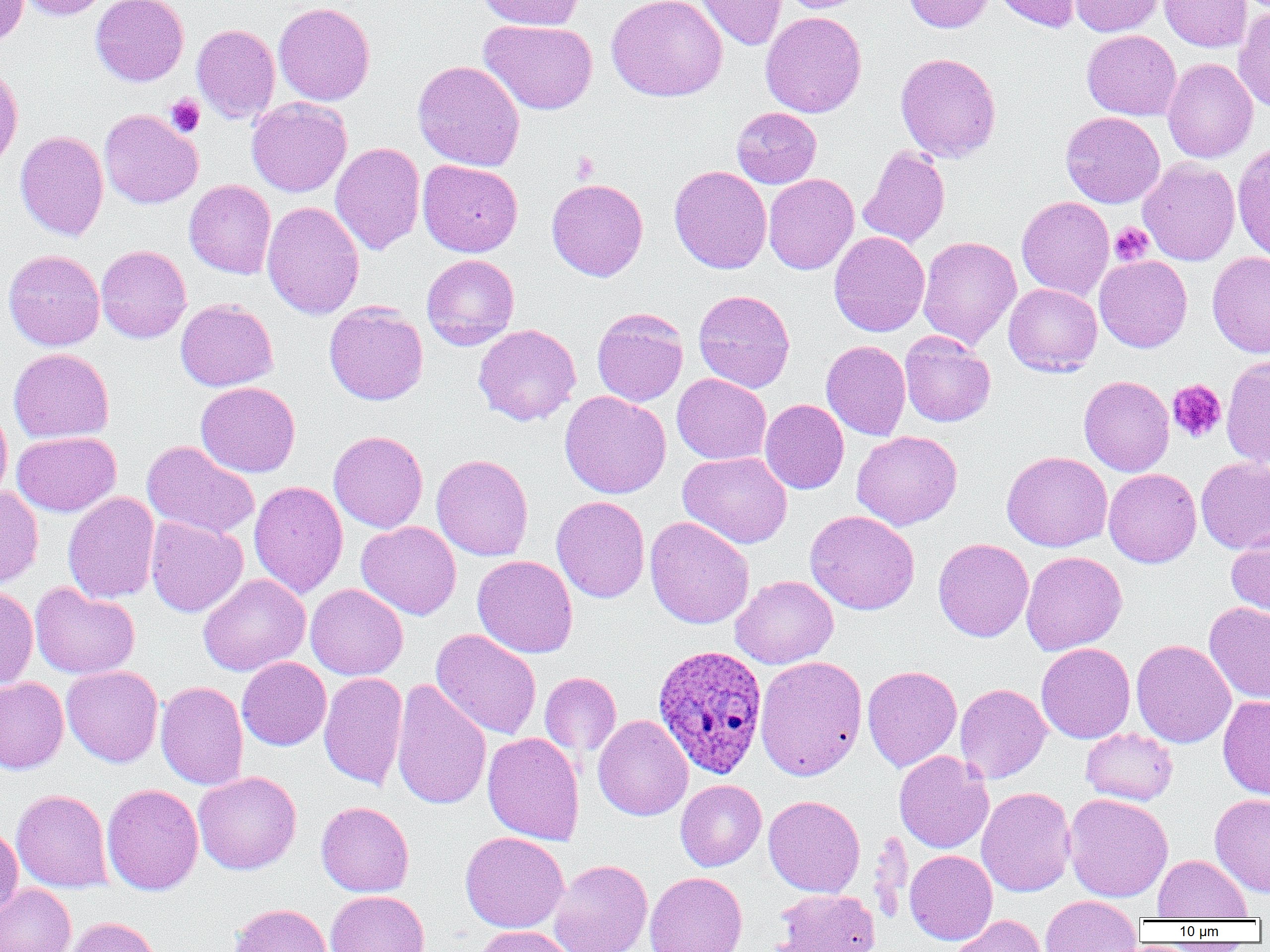

{
  "slide_level_diagnosis": "Plasmodium ovale",
  "image_size": "1270×952 pixels",
  "plasmodium_ovale_infected_red_blood_cell_locations": "approximate bounding boxes as [x1, y1, x2, y2] in pixels: [652, 644, 768, 778]",
  "uninfected_red_blood_cell_locations": "approximate bounding boxes as [x1, y1, x2, y2] in pixels: [0, 0, 29, 48], [18, 0, 112, 21], [91, 0, 189, 86], [477, 0, 585, 30], [606, 0, 728, 102], [696, 0, 787, 50], [778, 0, 872, 13], [902, 0, 995, 34], [993, 0, 1082, 32], [1070, 0, 1166, 36], [1159, 0, 1252, 52], [273, 2, 375, 106], [1234, 7, 1270, 112], [760, 11, 867, 118], [479, 19, 598, 115], [192, 24, 280, 123], [1082, 30, 1181, 120], [895, 52, 1002, 162], [1162, 58, 1258, 163], [413, 60, 525, 171], [0, 63, 23, 173], [247, 97, 352, 198], [731, 107, 822, 188], [99, 109, 203, 208], [1061, 111, 1165, 208], [15, 130, 108, 241], [330, 142, 425, 255], [1233, 145, 1270, 261], [858, 146, 950, 248], [1138, 158, 1240, 266], [417, 159, 523, 257], [669, 165, 772, 274], [763, 173, 859, 275], [546, 178, 648, 281], [184, 180, 276, 279], [1016, 196, 1114, 300], [262, 201, 365, 319], [829, 231, 930, 337], [917, 236, 1021, 350], [96, 245, 191, 343], [3, 250, 105, 351], [1207, 251, 1270, 357], [421, 254, 519, 350], [1094, 255, 1192, 353], [1004, 283, 1102, 376], [693, 289, 795, 392], [175, 298, 278, 391], [324, 302, 428, 405], [592, 308, 689, 407], [473, 324, 581, 426], [900, 331, 996, 427], [821, 341, 911, 440], [8, 348, 114, 443], [1221, 355, 1270, 467], [672, 373, 771, 464], [1079, 375, 1174, 476], [196, 381, 300, 477], [560, 391, 671, 499], [760, 399, 849, 494], [0, 403, 12, 504], [852, 430, 963, 530], [12, 431, 121, 516], [329, 431, 428, 533], [142, 441, 260, 540], [1002, 451, 1112, 552], [678, 452, 792, 548], [431, 454, 533, 561], [1196, 457, 1270, 554], [1104, 468, 1201, 568], [249, 480, 348, 598], [0, 486, 43, 589], [63, 492, 160, 604], [551, 496, 650, 603], [805, 510, 920, 615], [145, 515, 248, 617], [645, 516, 754, 629], [356, 521, 461, 620], [1226, 528, 1270, 619], [933, 538, 1034, 642], [1021, 551, 1127, 655], [472, 555, 578, 658], [198, 574, 311, 676], [730, 575, 839, 669], [29, 582, 140, 679], [305, 584, 408, 680], [0, 587, 38, 689], [1204, 601, 1270, 703], [431, 629, 542, 740], [1131, 639, 1236, 748], [1036, 642, 1135, 743], [754, 655, 867, 780], [237, 657, 331, 750], [62, 665, 164, 767], [862, 665, 962, 772], [539, 672, 621, 757], [319, 673, 409, 790], [0, 678, 69, 774], [391, 678, 491, 810], [155, 681, 248, 790], [955, 683, 1051, 783], [1218, 694, 1270, 799], [593, 715, 693, 821], [1080, 728, 1178, 805], [482, 732, 585, 846], [894, 751, 994, 854], [193, 771, 301, 874], [675, 779, 766, 871], [101, 783, 203, 895], [976, 786, 1076, 897], [11, 789, 112, 892], [1210, 792, 1270, 897], [1064, 793, 1173, 902], [763, 795, 865, 897], [316, 801, 414, 897], [0, 825, 23, 919], [868, 830, 913, 924], [460, 831, 569, 933], [905, 849, 998, 944], [1153, 854, 1252, 920], [549, 859, 653, 952], [645, 872, 747, 952], [0, 883, 76, 952], [773, 889, 881, 952], [325, 890, 430, 952], [1039, 895, 1142, 951], [228, 902, 331, 952], [949, 915, 1046, 952], [66, 917, 161, 952], [476, 925, 575, 952]",
  "field_of_view": "single",
  "platelet_locations": "approximate bounding boxes as [x1, y1, x2, y2] in pixels: [165, 94, 206, 136], [571, 152, 600, 183], [1109, 222, 1153, 266], [1167, 378, 1227, 443]",
  "magnification": "1000x",
  "modality": "light microscopy",
  "preparation": "thin blood smear"
}